Identify the blood parasite species.
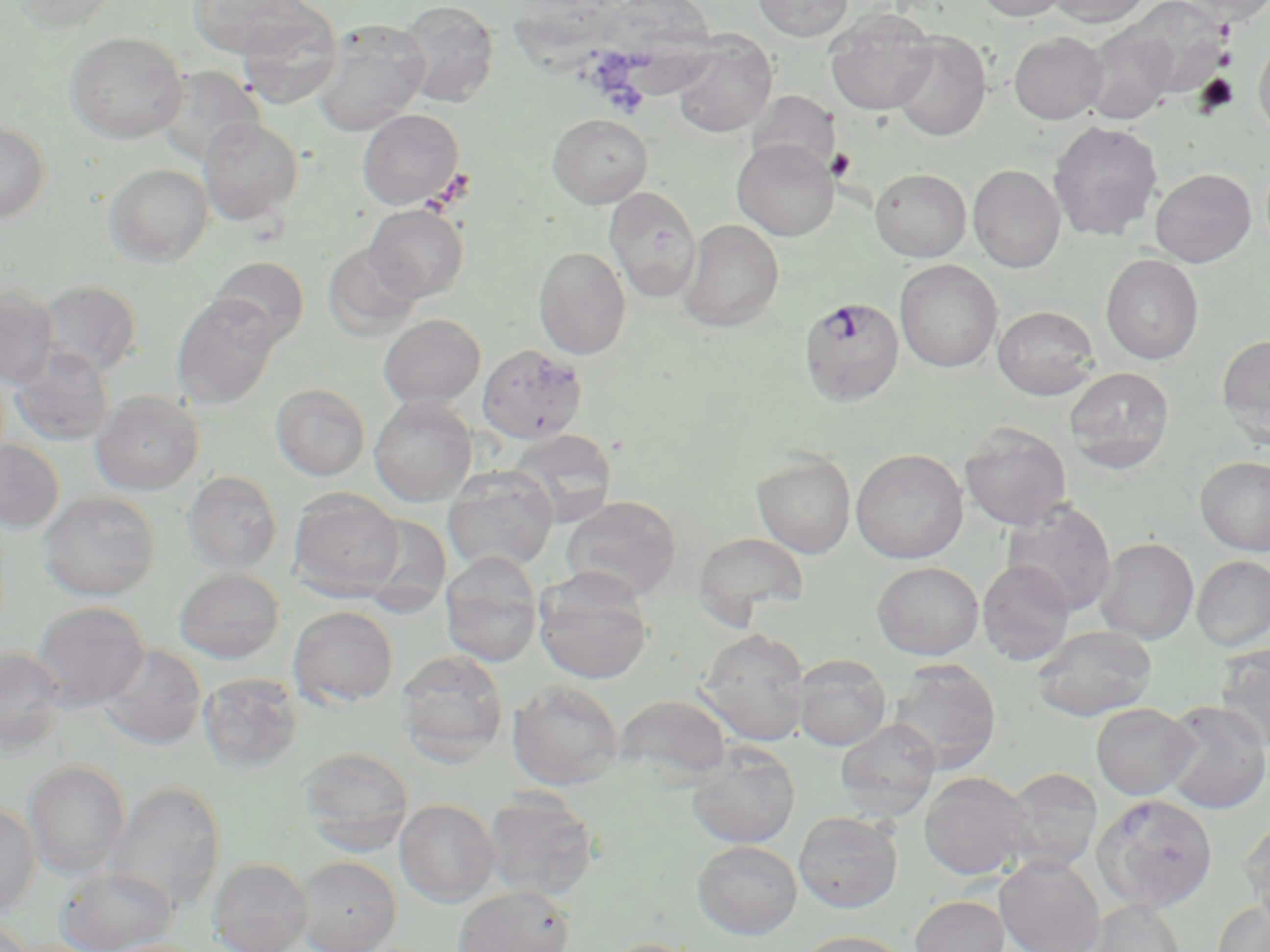

Plasmodium falciparum.

Summary:
  - Coordinate format: approximate bounding boxes as [x1, y1, x2, y2] in pixels
  - Platelet locations: [1215, 48, 1237, 68], [826, 147, 857, 183]
  - Uninfected red blood cell locations: [13, 0, 120, 34], [189, 0, 316, 58], [513, 0, 622, 82], [753, 0, 853, 41], [973, 0, 1069, 21], [1047, 0, 1149, 27], [1127, 0, 1231, 98], [1181, 0, 1270, 25], [397, 1, 499, 108], [600, 2, 717, 101], [236, 8, 342, 110], [825, 10, 938, 115], [311, 20, 431, 136], [1083, 22, 1177, 124], [65, 32, 188, 143], [891, 32, 991, 141], [1009, 32, 1108, 124], [671, 34, 777, 137], [1254, 35, 1270, 142], [154, 65, 264, 166], [748, 91, 840, 176], [358, 108, 464, 210], [548, 114, 653, 208], [198, 117, 303, 225], [1048, 120, 1163, 241], [0, 121, 50, 223], [732, 138, 839, 240], [104, 164, 213, 266], [968, 164, 1066, 273], [870, 168, 971, 261], [1150, 168, 1256, 267], [605, 187, 701, 302], [365, 204, 468, 301], [679, 219, 784, 332], [323, 243, 423, 340], [533, 246, 631, 360], [1101, 253, 1204, 364], [207, 256, 309, 349], [895, 259, 1002, 373], [38, 279, 142, 377], [0, 287, 59, 387], [172, 295, 280, 409], [992, 305, 1100, 400], [378, 314, 486, 408], [1217, 334, 1270, 442], [7, 345, 114, 446], [1064, 366, 1175, 473], [271, 384, 370, 480], [91, 390, 204, 495], [370, 396, 477, 506], [960, 425, 1071, 529], [508, 428, 618, 526], [0, 440, 64, 534], [851, 449, 968, 564], [752, 452, 856, 558], [1196, 457, 1270, 556], [442, 466, 558, 573], [183, 471, 282, 574], [288, 488, 404, 599], [39, 491, 160, 600], [560, 495, 682, 602], [1002, 500, 1116, 616], [357, 514, 452, 617], [693, 532, 809, 622], [1094, 537, 1199, 643], [439, 552, 544, 667], [1192, 555, 1270, 651], [977, 559, 1075, 666], [872, 561, 984, 659], [174, 568, 284, 663], [533, 572, 653, 685], [31, 600, 150, 709], [288, 606, 399, 708], [1031, 625, 1158, 721], [697, 628, 812, 746], [98, 644, 206, 750], [1214, 644, 1270, 748], [0, 646, 66, 754], [395, 649, 509, 766], [791, 656, 891, 751], [888, 660, 1001, 773], [198, 672, 303, 773], [507, 680, 624, 790], [501, 681, 613, 900], [614, 693, 732, 784], [1161, 701, 1270, 814], [1091, 703, 1198, 800], [835, 719, 941, 820], [299, 747, 414, 853], [686, 748, 800, 848], [23, 760, 130, 878], [1000, 768, 1103, 874], [919, 771, 1035, 880], [107, 781, 226, 912], [483, 791, 600, 901], [1093, 793, 1218, 912], [395, 799, 500, 907], [0, 802, 41, 916], [793, 810, 903, 912], [1239, 817, 1270, 918], [692, 839, 802, 939], [996, 855, 1105, 952], [293, 856, 401, 952], [208, 857, 313, 952], [54, 865, 177, 951], [453, 885, 574, 952], [910, 896, 1008, 952], [1088, 899, 1186, 952], [1212, 900, 1270, 952], [0, 916, 36, 952], [795, 931, 910, 952], [596, 937, 707, 952]
  - Plasmodium falciparum-infected red blood cell locations: [799, 296, 904, 406], [477, 344, 588, 444]
  - Preparation: thin blood smear
  - Field of view: single
  - Modality: optical microscopy
  - Magnification: 1000x
  - Image size: 1270×952 pixels
  - Stain: May-Grünwald-Giemsa